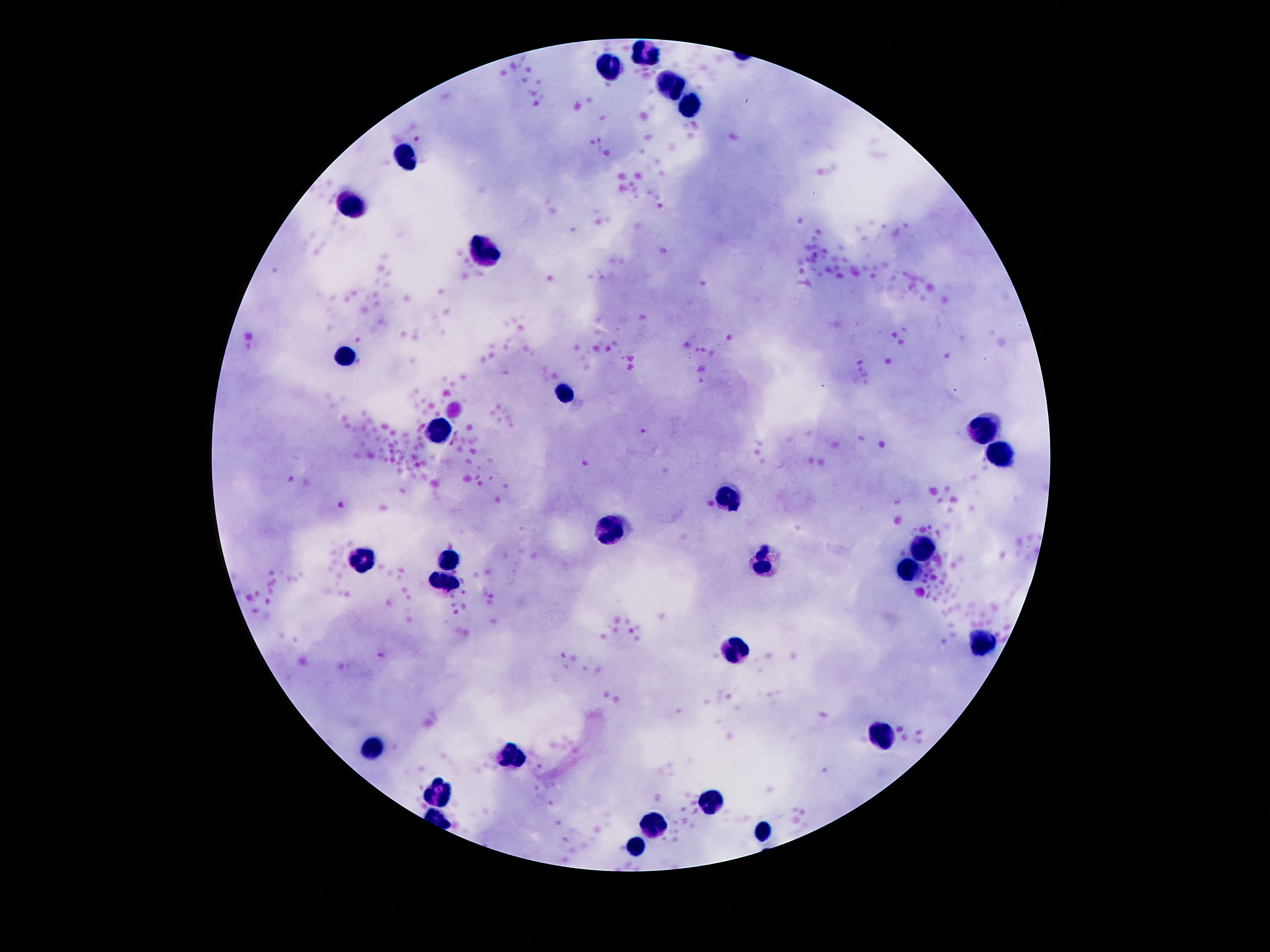
capture = smartphone camera through the microscope eyepiece
stain = Giemsa
field of view = single
magnification = 100x
preparation = thick blood smear
patient malaria status = not infected
image size = 1270×952 pixels
leukocyte locations = approximate centers as {x, y} in pixels: {643, 57}, {606, 67}, {669, 85}, {690, 107}, {404, 156}, {354, 199}, {486, 249}, {346, 356}, {563, 393}, {438, 432}, {983, 434}, {999, 452}, {729, 499}, {611, 529}, {923, 546}, {361, 559}, {451, 561}, {764, 565}, {910, 570}, {979, 642}, {736, 648}, {884, 734}, {380, 749}, {514, 758}, {438, 793}, {712, 806}, {658, 824}, {761, 827}, {632, 849}